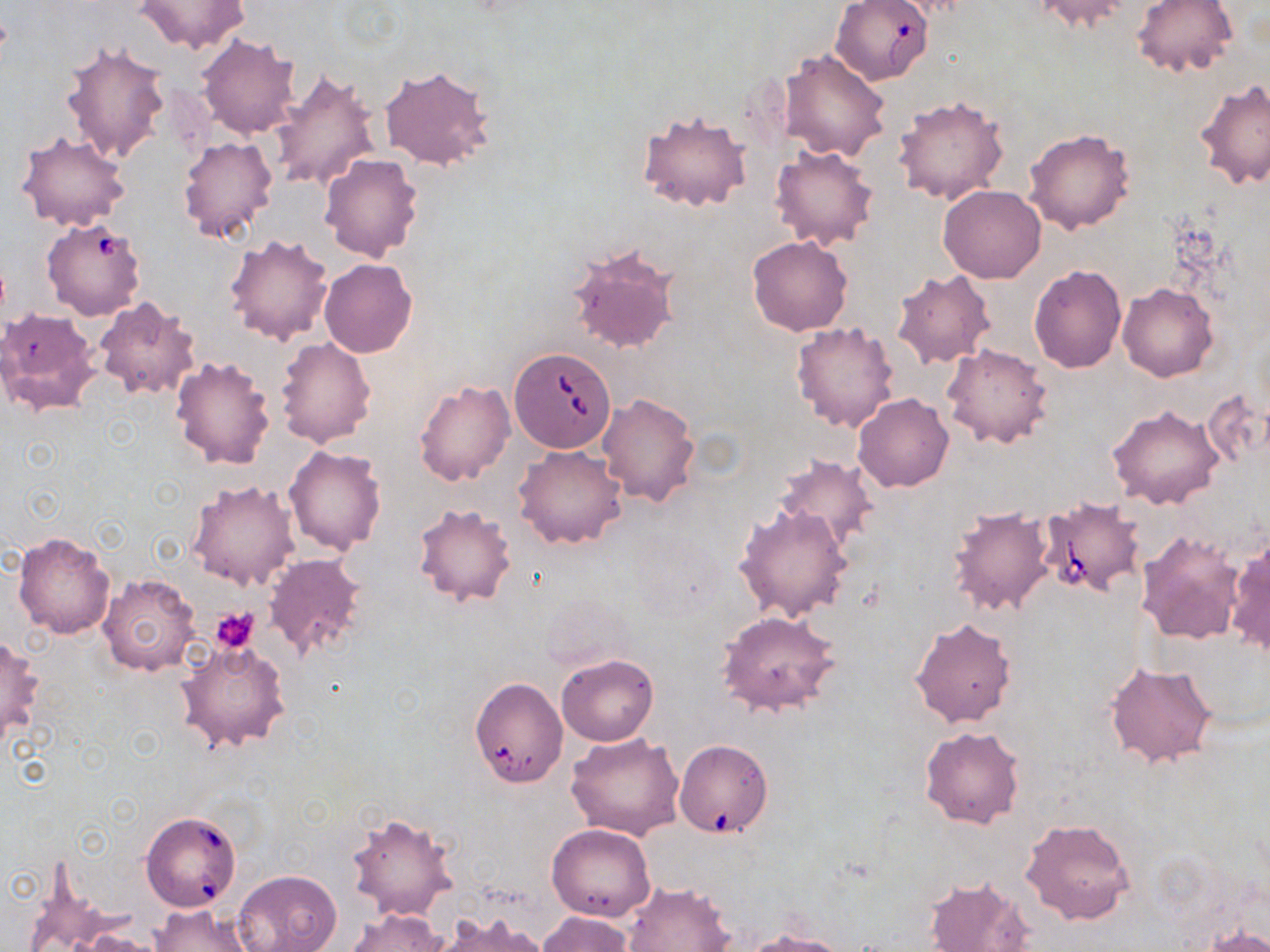 Approximate bounding boxes as (x1, y1, x2, y2) in pixels. Platelet locations: (211, 607, 259, 652). Uninfected red blood cell locations: (1026, 0, 1135, 34), (1133, 0, 1236, 79), (134, 1, 250, 53), (196, 33, 301, 139), (61, 42, 172, 165), (779, 48, 891, 161), (380, 64, 496, 172), (269, 68, 382, 193), (1195, 78, 1270, 190), (894, 95, 1009, 206), (637, 108, 752, 213), (1025, 129, 1133, 234), (16, 132, 130, 231), (178, 135, 279, 243), (769, 145, 881, 251), (319, 153, 425, 263), (938, 185, 1047, 282), (225, 233, 333, 345), (747, 236, 853, 336), (568, 245, 681, 357), (319, 258, 417, 358), (1028, 264, 1127, 373), (891, 269, 996, 370), (1118, 282, 1218, 382), (91, 297, 199, 401), (0, 307, 100, 414), (791, 322, 901, 432), (275, 336, 376, 446), (943, 343, 1053, 449), (170, 355, 276, 470), (414, 381, 515, 486), (596, 392, 700, 509), (853, 393, 954, 492), (1107, 402, 1225, 508), (284, 444, 387, 557), (514, 446, 628, 550), (773, 455, 880, 552), (187, 480, 300, 589), (412, 503, 518, 607), (735, 503, 855, 623), (947, 504, 1058, 618), (1136, 530, 1245, 645), (12, 531, 116, 639), (1225, 535, 1269, 661), (263, 555, 368, 664), (98, 574, 202, 675), (716, 610, 842, 717), (908, 616, 1018, 730), (0, 633, 44, 745), (175, 635, 289, 755), (557, 654, 658, 746), (1104, 661, 1219, 769), (474, 679, 568, 785), (919, 725, 1026, 829), (566, 732, 684, 840), (676, 740, 772, 840), (347, 810, 459, 922), (1020, 817, 1135, 925), (546, 823, 656, 922), (232, 870, 341, 952), (24, 873, 114, 952), (922, 876, 1034, 952), (622, 880, 734, 951), (149, 903, 251, 952), (345, 908, 448, 952), (538, 911, 635, 952), (431, 913, 552, 952), (1203, 925, 1270, 952), (74, 930, 166, 952), (741, 931, 854, 952). Babesia divergens-infected red blood cell locations: (830, 0, 934, 85), (42, 217, 147, 321), (508, 346, 618, 453), (1037, 497, 1143, 601), (141, 810, 242, 912). Slide-level diagnosis: Babesia divergens. Optical microscopy. May-Grünwald-Giemsa-stained preparation. Image is 1270×952 pixels. Single field of view. Thin blood film. Captured at 1000x magnification.